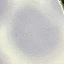
{
  "result": "no malaria parasites detected",
  "image_type": "automatically extracted cell patch, resized to 64 × 64 pixels",
  "capture": "smartphone through the microscope eyepiece",
  "stain": "Giemsa",
  "preparation": "thin blood smear"
}